Evaluate for malaria.
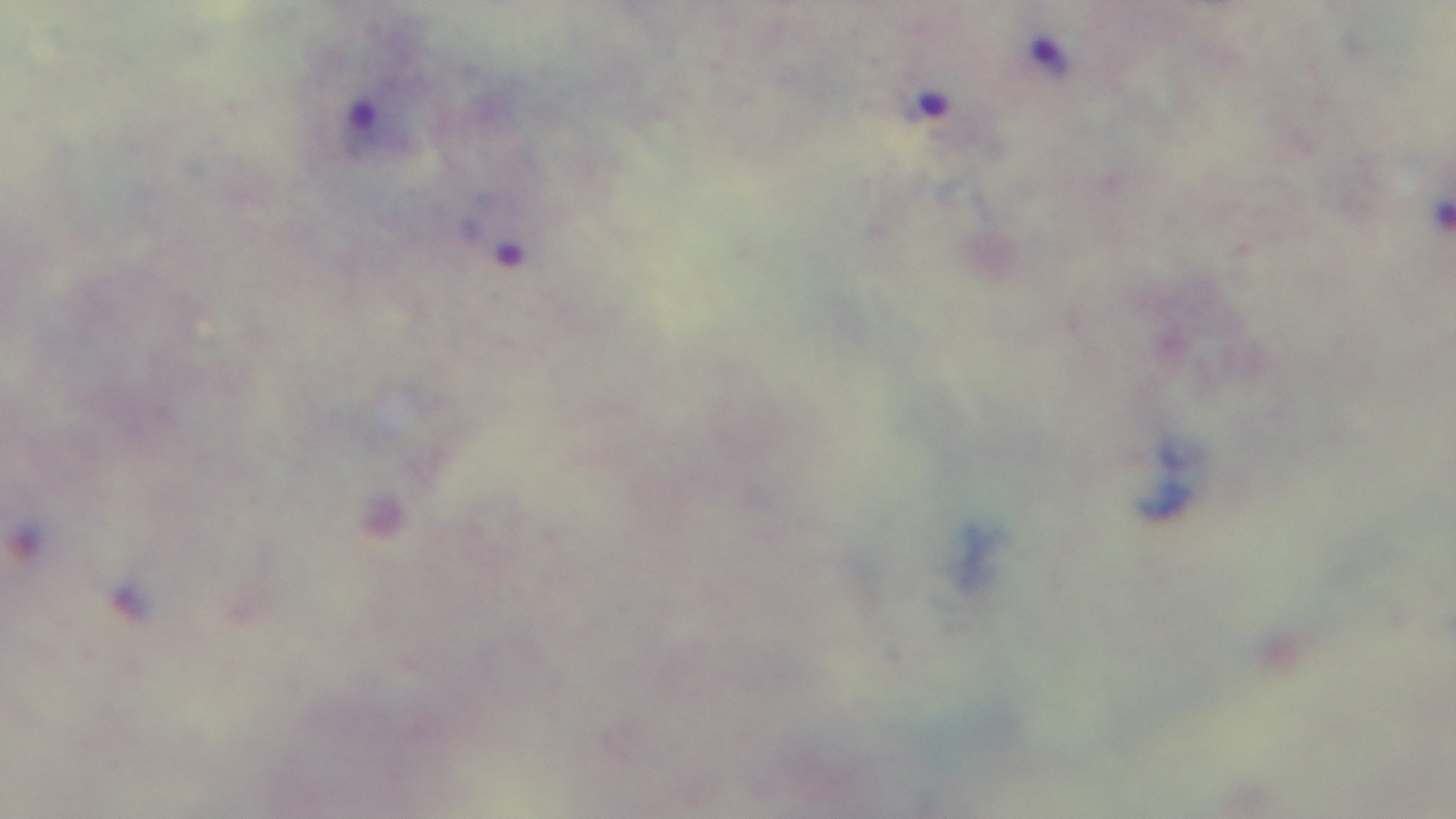
Infected.

Mounted 4K digital camera. Giemsa-stained. Single field of view. 100x oil-immersion objective. Photomicrograph. Preparation: thick smear.